Give the extent of all uninfected red blood cells.
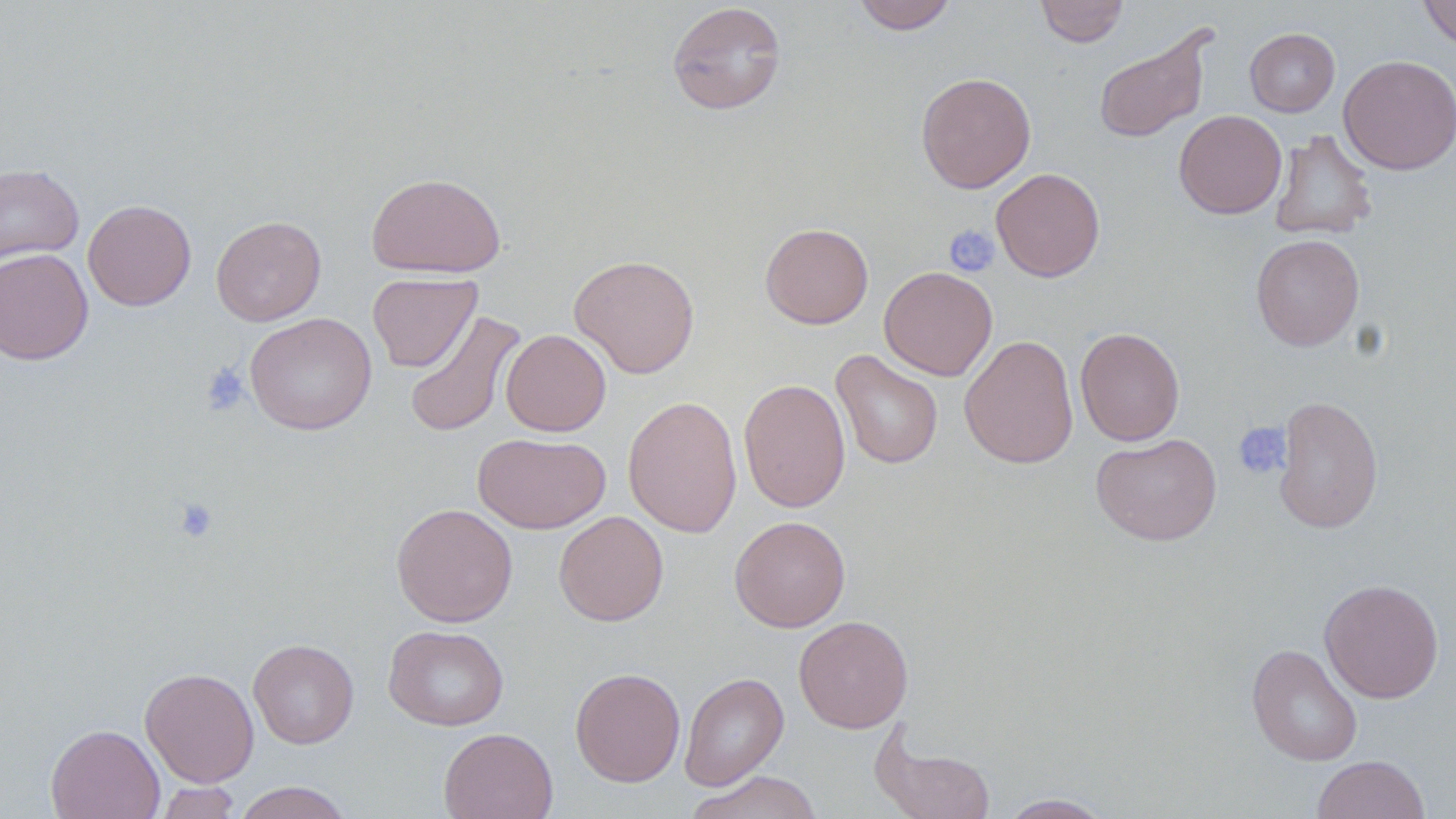
Approximate bounding boxes as (x1,y1)-(x2,y2) corner pairs in pixels.
Uninfected red blood cells: (852,0)-(958,34), (1035,0)-(1130,47), (1418,0)-(1456,51), (667,2)-(787,115), (1093,26)-(1214,143), (1244,27)-(1340,117), (1338,54)-(1456,175), (916,72)-(1036,193), (1173,109)-(1287,219), (1269,129)-(1377,241), (0,164)-(84,264), (991,168)-(1105,282), (366,172)-(506,278), (82,199)-(196,311), (211,215)-(326,326), (759,222)-(873,329), (1251,233)-(1364,351), (0,247)-(93,365), (568,254)-(700,379), (879,266)-(997,381), (367,272)-(481,372), (403,310)-(526,438), (244,312)-(377,435), (1075,326)-(1185,445), (500,329)-(611,436), (959,334)-(1079,469), (831,350)-(943,470), (738,378)-(850,513), (623,395)-(742,538), (1273,395)-(1384,534), (1090,432)-(1222,546), (473,433)-(611,534), (391,503)-(518,627), (554,510)-(668,626), (729,515)-(850,633), (1319,578)-(1444,703), (793,615)-(913,733), (383,624)-(509,731), (249,638)-(359,748), (1246,643)-(1363,766), (140,667)-(260,787), (570,667)-(685,787), (679,672)-(789,790), (46,724)-(164,819), (438,727)-(558,819), (872,727)-(996,819), (1312,755)-(1430,818), (686,770)-(823,819), (152,781)-(242,819), (232,782)-(353,819), (998,793)-(1113,818).

Platelet locations: (943,223)-(1000,278), (201,363)-(250,416), (1232,422)-(1292,480), (172,496)-(219,543). Slide-level diagnosis: no evidence of blood parasites. One field of a larger specimen. 1000x magnification. Image is 1456×819 pixels. Thin blood film. May-Grünwald-Giemsa-stained preparation. Optical microscopy.